Report the malaria status of this cell.
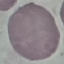
Uninfected.

Automatically extracted cell patch, resized to 64 × 64 pixels. Thin smear of blood. Giemsa-stained preparation. Acquired by smartphone through the microscope eyepiece.